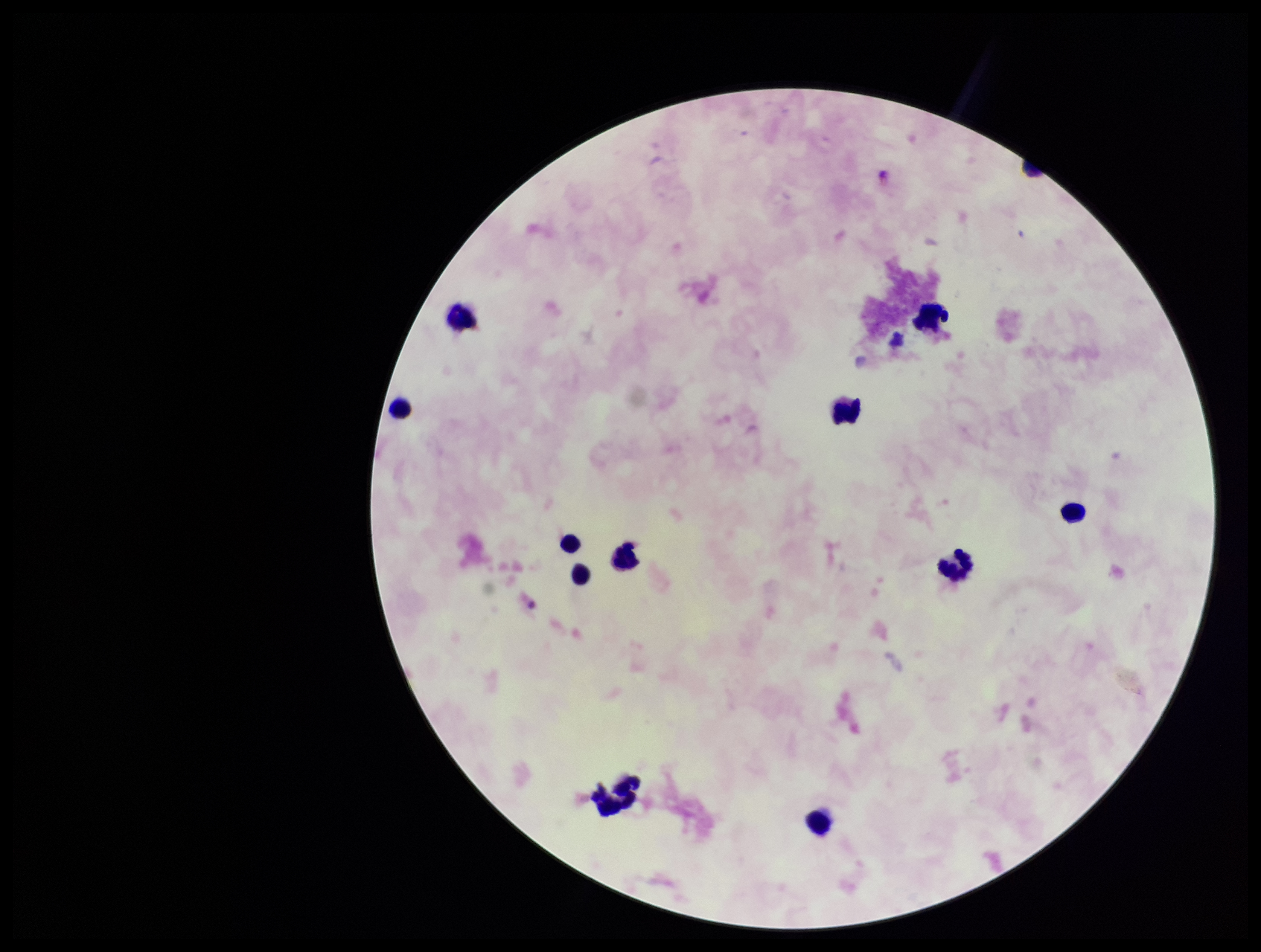 Parasite count: 0. Image is 1261×952 pixels. Leukocyte count: 11. Plasmodium parasites: none identified. Preparation: thick. Single field of view. Stained with Giemsa. Patient malaria status: negative. Photographed through the microscope eyepiece with a smartphone camera.